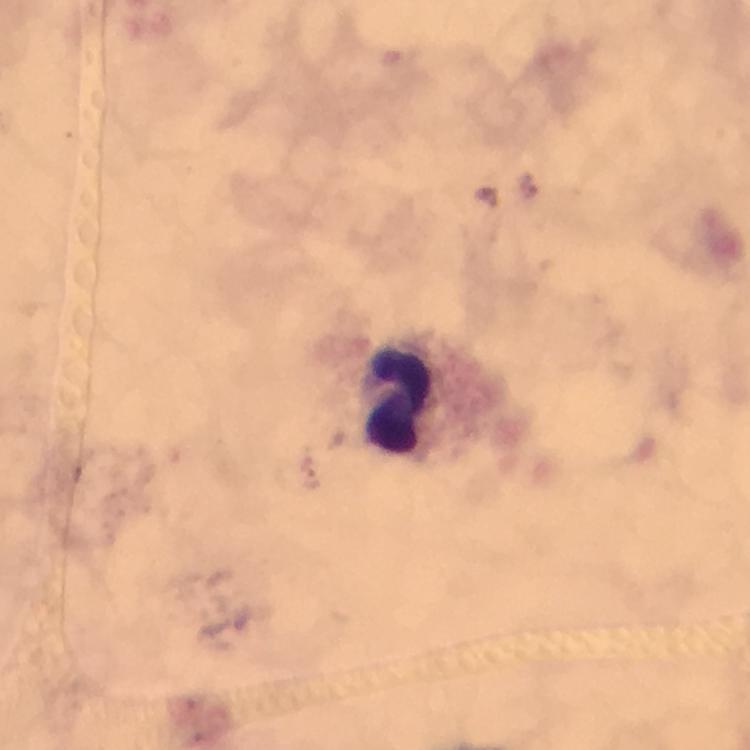

Approximate centers as (x, y) in pixels. Leukocyte locations: (402, 398). Malaria parasite locations: (529, 185), (311, 479). Thick smear. Image is 750×750 pixels. Giemsa stain. At 100x magnification. From a malaria diagnostic workup. Cropped region of a single field of view. Photographed through the microscope with a smartphone camera. Immersion oil was used.